Outline each Plasmodium falciparum-infected red blood cell.
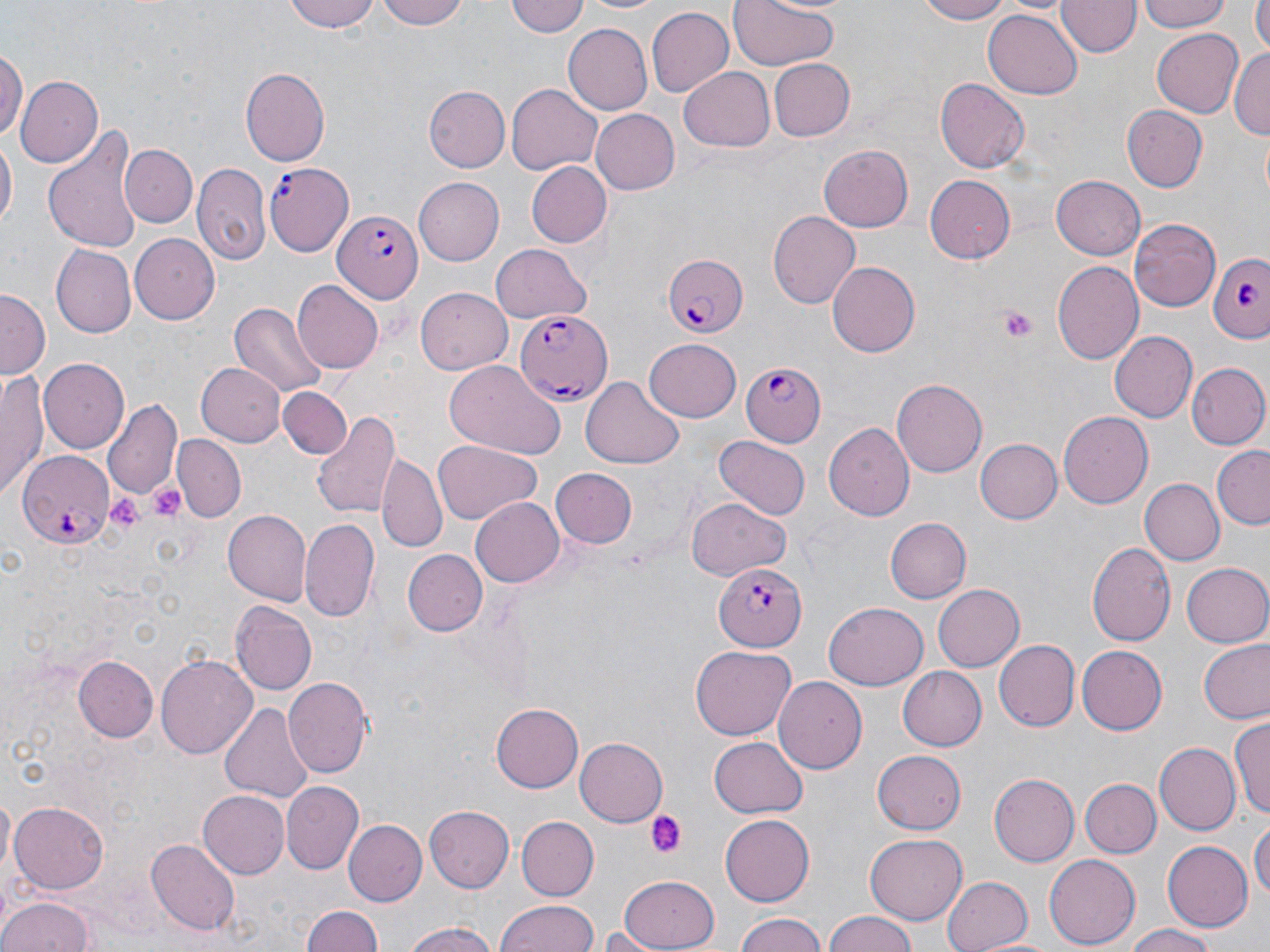
Approximate bounding boxes as named x1/y1/x2/y2 corners in pixels.
Plasmodium falciparum-infected red blood cells: (x1=264, y1=156, x2=360, y2=258), (x1=333, y1=208, x2=421, y2=302), (x1=1209, y1=252, x2=1270, y2=343), (x1=660, y1=254, x2=749, y2=339), (x1=516, y1=311, x2=611, y2=404), (x1=739, y1=362, x2=826, y2=447), (x1=15, y1=450, x2=115, y2=548), (x1=714, y1=560, x2=806, y2=651).

slide_level_diagnosis: Plasmodium falciparum
uninfected_red_blood_cell_locations: 'approximate bounding boxes as named x1/y1/x2/y2 corners in pixels: (x1=287, y1=0, x2=382, y2=33), (x1=377, y1=0, x2=466, y2=29), (x1=506, y1=0, x2=589, y2=39), (x1=577, y1=0, x2=675, y2=16), (x1=727, y1=0, x2=842, y2=71), (x1=914, y1=0, x2=1013, y2=24), (x1=1139, y1=0, x2=1230, y2=34), (x1=1252, y1=0, x2=1270, y2=53), (x1=1056, y1=1, x2=1140, y2=59), (x1=645, y1=6, x2=734, y2=98), (x1=983, y1=6, x2=1084, y2=99), (x1=564, y1=23, x2=653, y2=113), (x1=1150, y1=28, x2=1245, y2=118), (x1=0, y1=45, x2=26, y2=143), (x1=1230, y1=45, x2=1270, y2=143), (x1=769, y1=59, x2=855, y2=142), (x1=239, y1=67, x2=330, y2=166), (x1=680, y1=68, x2=774, y2=150), (x1=15, y1=75, x2=101, y2=170), (x1=934, y1=77, x2=1029, y2=171), (x1=508, y1=83, x2=603, y2=174), (x1=424, y1=86, x2=510, y2=172), (x1=1124, y1=105, x2=1208, y2=192), (x1=592, y1=109, x2=681, y2=195), (x1=43, y1=127, x2=140, y2=251), (x1=1, y1=137, x2=16, y2=236), (x1=819, y1=143, x2=914, y2=231), (x1=121, y1=144, x2=196, y2=228), (x1=527, y1=163, x2=610, y2=246), (x1=193, y1=164, x2=270, y2=267), (x1=1051, y1=175, x2=1147, y2=260), (x1=924, y1=176, x2=1017, y2=264), (x1=414, y1=178, x2=504, y2=265), (x1=768, y1=210, x2=861, y2=308), (x1=1128, y1=218, x2=1222, y2=310), (x1=130, y1=232, x2=220, y2=325), (x1=488, y1=243, x2=593, y2=324), (x1=52, y1=244, x2=136, y2=338), (x1=829, y1=260, x2=921, y2=357), (x1=1053, y1=261, x2=1144, y2=366), (x1=293, y1=281, x2=384, y2=374), (x1=0, y1=287, x2=50, y2=376), (x1=417, y1=289, x2=513, y2=374), (x1=228, y1=303, x2=328, y2=398), (x1=1108, y1=330, x2=1196, y2=423), (x1=644, y1=335, x2=741, y2=419), (x1=40, y1=359, x2=129, y2=452), (x1=198, y1=361, x2=287, y2=447), (x1=444, y1=361, x2=560, y2=459), (x1=1185, y1=363, x2=1269, y2=451), (x1=1, y1=368, x2=51, y2=499), (x1=582, y1=376, x2=684, y2=469), (x1=892, y1=379, x2=988, y2=476), (x1=278, y1=387, x2=350, y2=458), (x1=103, y1=399, x2=183, y2=503), (x1=1058, y1=409, x2=1153, y2=505), (x1=311, y1=410, x2=401, y2=521), (x1=824, y1=423, x2=914, y2=521), (x1=173, y1=436, x2=245, y2=520), (x1=713, y1=436, x2=810, y2=522), (x1=977, y1=439, x2=1061, y2=524), (x1=433, y1=441, x2=541, y2=525), (x1=1212, y1=446, x2=1270, y2=529), (x1=377, y1=457, x2=449, y2=552), (x1=550, y1=469, x2=638, y2=548), (x1=1138, y1=478, x2=1224, y2=566), (x1=471, y1=498, x2=564, y2=587), (x1=687, y1=498, x2=789, y2=580), (x1=221, y1=511, x2=310, y2=604), (x1=884, y1=517, x2=971, y2=603), (x1=301, y1=519, x2=380, y2=621), (x1=1086, y1=539, x2=1175, y2=647), (x1=404, y1=548, x2=489, y2=637), (x1=1182, y1=563, x2=1270, y2=647), (x1=933, y1=584, x2=1024, y2=672), (x1=233, y1=603, x2=317, y2=696), (x1=822, y1=603, x2=927, y2=690), (x1=995, y1=638, x2=1079, y2=731), (x1=1201, y1=639, x2=1270, y2=723), (x1=1076, y1=645, x2=1165, y2=735), (x1=691, y1=646, x2=796, y2=740), (x1=157, y1=652, x2=257, y2=759), (x1=75, y1=657, x2=158, y2=741), (x1=897, y1=665, x2=987, y2=751), (x1=773, y1=676, x2=865, y2=776), (x1=282, y1=677, x2=370, y2=778), (x1=219, y1=701, x2=315, y2=803), (x1=491, y1=703, x2=584, y2=792), (x1=1229, y1=718, x2=1269, y2=818), (x1=709, y1=735, x2=807, y2=816), (x1=576, y1=738, x2=668, y2=825), (x1=1153, y1=743, x2=1240, y2=837), (x1=871, y1=749, x2=967, y2=834), (x1=991, y1=772, x2=1080, y2=867), (x1=1080, y1=778, x2=1160, y2=857), (x1=282, y1=781, x2=364, y2=872), (x1=198, y1=790, x2=289, y2=879), (x1=10, y1=800, x2=110, y2=892), (x1=423, y1=805, x2=513, y2=894), (x1=720, y1=813, x2=816, y2=905), (x1=517, y1=816, x2=598, y2=899), (x1=1251, y1=817, x2=1270, y2=909), (x1=345, y1=820, x2=426, y2=904), (x1=865, y1=832, x2=966, y2=922), (x1=148, y1=840, x2=240, y2=936), (x1=1164, y1=840, x2=1251, y2=933), (x1=1043, y1=854, x2=1138, y2=950), (x1=616, y1=873, x2=720, y2=951), (x1=940, y1=874, x2=1032, y2=952), (x1=0, y1=895, x2=97, y2=952), (x1=494, y1=900, x2=600, y2=952), (x1=301, y1=907, x2=382, y2=952), (x1=821, y1=911, x2=919, y2=952), (x1=733, y1=913, x2=826, y2=952), (x1=401, y1=919, x2=505, y2=952), (x1=1122, y1=924, x2=1221, y2=952), (x1=596, y1=926, x2=670, y2=952)'
field_of_view: one of a larger specimen
stain: May-Grünwald-Giemsa
preparation: thin blood smear
image_size: 1270×952 pixels
modality: light microscopy
platelet_locations: 'approximate bounding boxes as named x1/y1/x2/y2 corners in pixels: (x1=995, y1=304, x2=1040, y2=339), (x1=147, y1=480, x2=185, y2=521), (x1=107, y1=496, x2=145, y2=534), (x1=644, y1=810, x2=688, y2=860)'
magnification: 1000x